Assess the morphology of the erythrocytes.
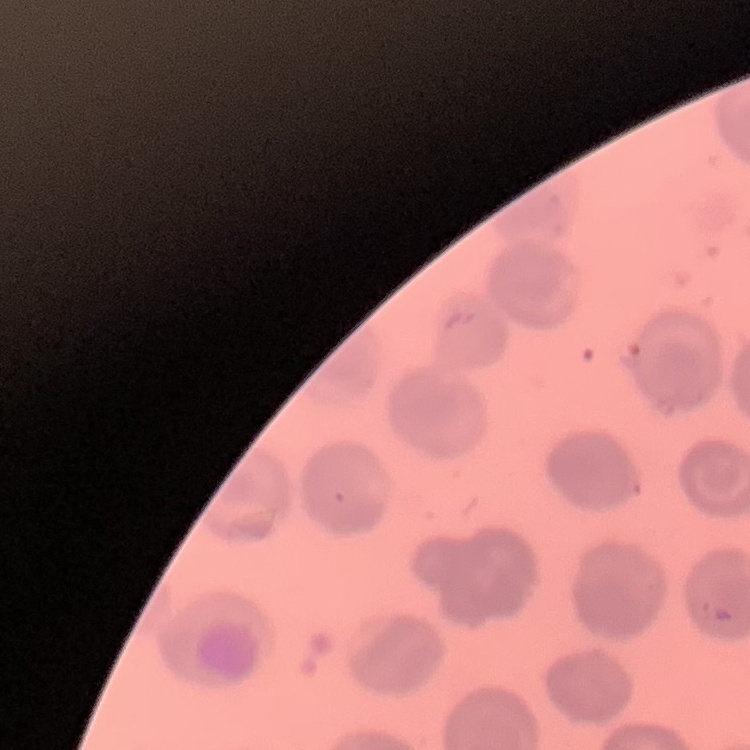

They show no rouleaux formation.

image type = one tile cut from a larger photomicrograph
preparation = thin blood smear
stain = Field's or Giemsa